Identify the preparation type.
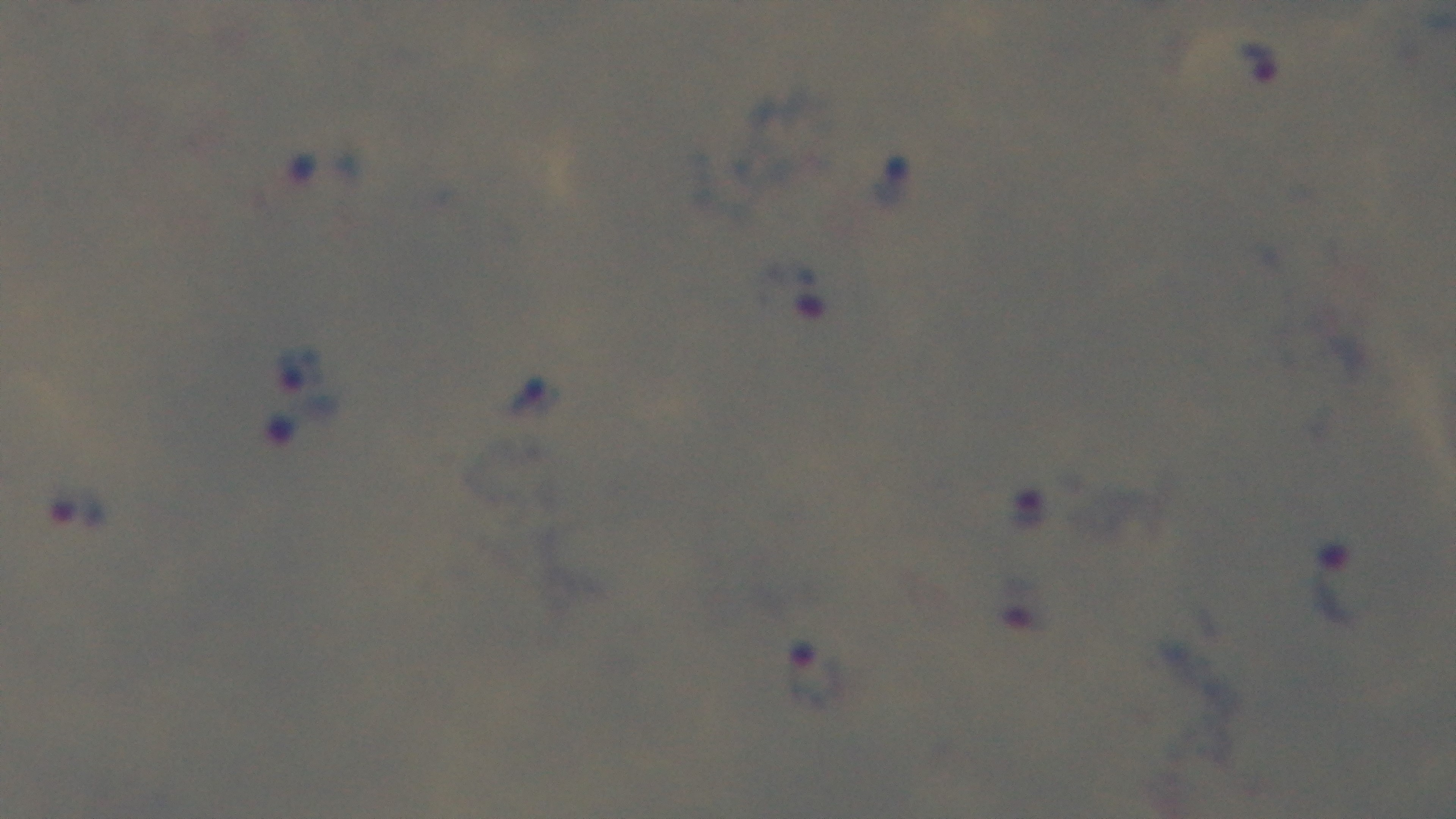

Thick.

Summary:
  - Stain: Giemsa
  - Modality: light microscopy
  - Capture: mounted 4K digital camera
  - Objective: 100x oil immersion
  - Malaria status: infected
  - Field of view: one from the slide